Assess this cell for malaria.
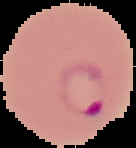

Parasitized.

Image is 136×148 pixels. Cell region segmented out of the field of view; the surrounding area is masked to black. From a thin blood smear.